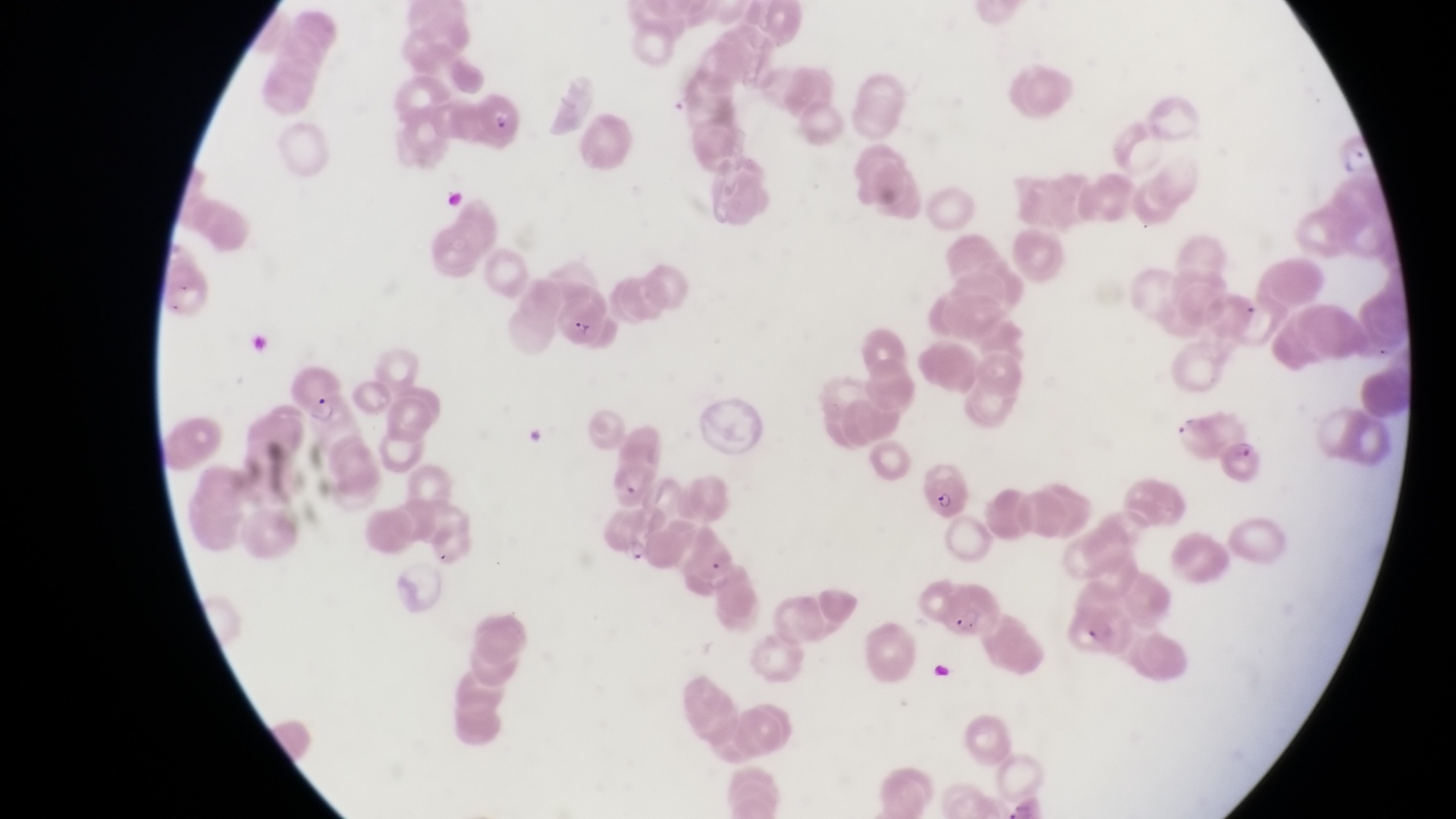

Approximate bounding boxes as [left, top, right, bottom] in pixels.
Summary:
  - Trophozoite locations: [1338, 143, 1370, 177]
  - Parasitised red blood cell locations: [469, 90, 528, 145], [555, 285, 610, 351], [291, 360, 355, 427], [1221, 429, 1268, 487], [917, 455, 975, 521], [594, 505, 660, 565], [938, 589, 1007, 652]
  - Capture: smartphone photograph through the eyepiece of an Olympus CX-23 microscope
  - Field of view: single
  - Preparation: thin blood film
  - Country: Uganda
  - Magnification: 1000x
  - Image size: 1456×819 pixels